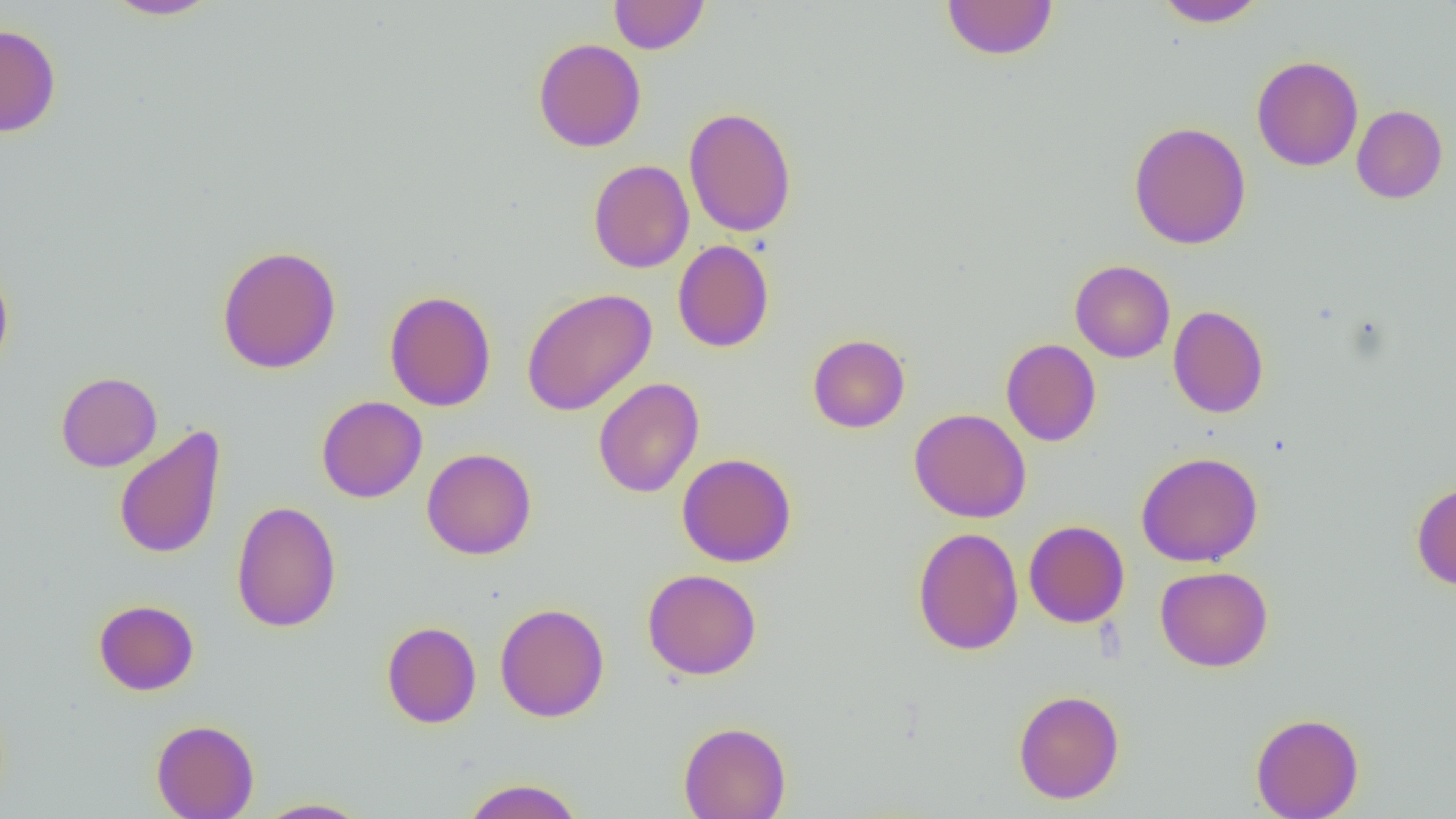

Summary:
  - Coordinate format: approximate bounding boxes as [x1, y1, x2, y2] in pixels
  - Uninfected red blood cell locations: [102, 0, 221, 20], [608, 0, 710, 54], [941, 0, 1058, 60], [1153, 0, 1269, 28], [0, 24, 61, 138], [533, 38, 646, 152], [1252, 55, 1363, 171], [1352, 105, 1448, 203], [683, 106, 797, 238], [1129, 121, 1251, 250], [588, 159, 694, 273], [673, 240, 775, 353], [216, 245, 342, 374], [0, 260, 14, 377], [1070, 260, 1175, 362], [521, 287, 657, 416], [384, 290, 496, 411], [1168, 305, 1269, 418], [808, 334, 910, 433], [1001, 338, 1101, 446], [56, 371, 162, 472], [593, 377, 704, 498], [316, 396, 427, 503], [909, 408, 1031, 523], [113, 425, 227, 561], [422, 448, 537, 560], [1136, 451, 1264, 568], [677, 452, 797, 567], [1411, 480, 1456, 590], [231, 500, 341, 633], [1024, 520, 1129, 628], [912, 527, 1024, 655], [1155, 565, 1274, 672], [642, 568, 762, 680], [93, 599, 199, 695], [495, 603, 609, 723], [381, 621, 481, 728], [1013, 689, 1124, 804], [1250, 712, 1364, 819], [151, 718, 259, 819], [678, 721, 792, 819], [461, 777, 584, 819], [254, 798, 374, 818]
  - Slide-level diagnosis: negative for blood parasites
  - Field of view: one of a larger specimen
  - Image size: 1456×819 pixels
  - Modality: light microscopy
  - Preparation: thin blood smear
  - Magnification: 1000x